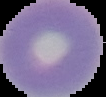

Cell region segmented out of the field of view; the surrounding area is masked to black. Image is 106×97 pixels. Malaria status: uninfected. From a thin blood smear.